Report the malaria status of this cell.
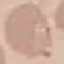
It is uninfected.

{
  "stain": "Giemsa",
  "capture": "smartphone camera at the microscope eyepiece",
  "image_type": "automatically extracted cell patch, resized to 64 × 64 pixels",
  "preparation": "thin smear"
}